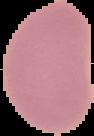
Summary:
  - Malaria status: uninfected
  - Preparation: thin blood film
  - Image type: segmented cell region on a black background
  - Image size: 94×136 pixels